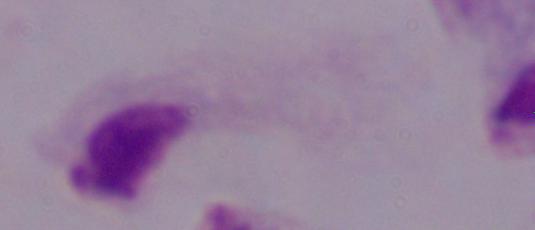

A trichomonad is shown. Micrograph. 1000x magnification.